Outline each blood parasite and name the species.
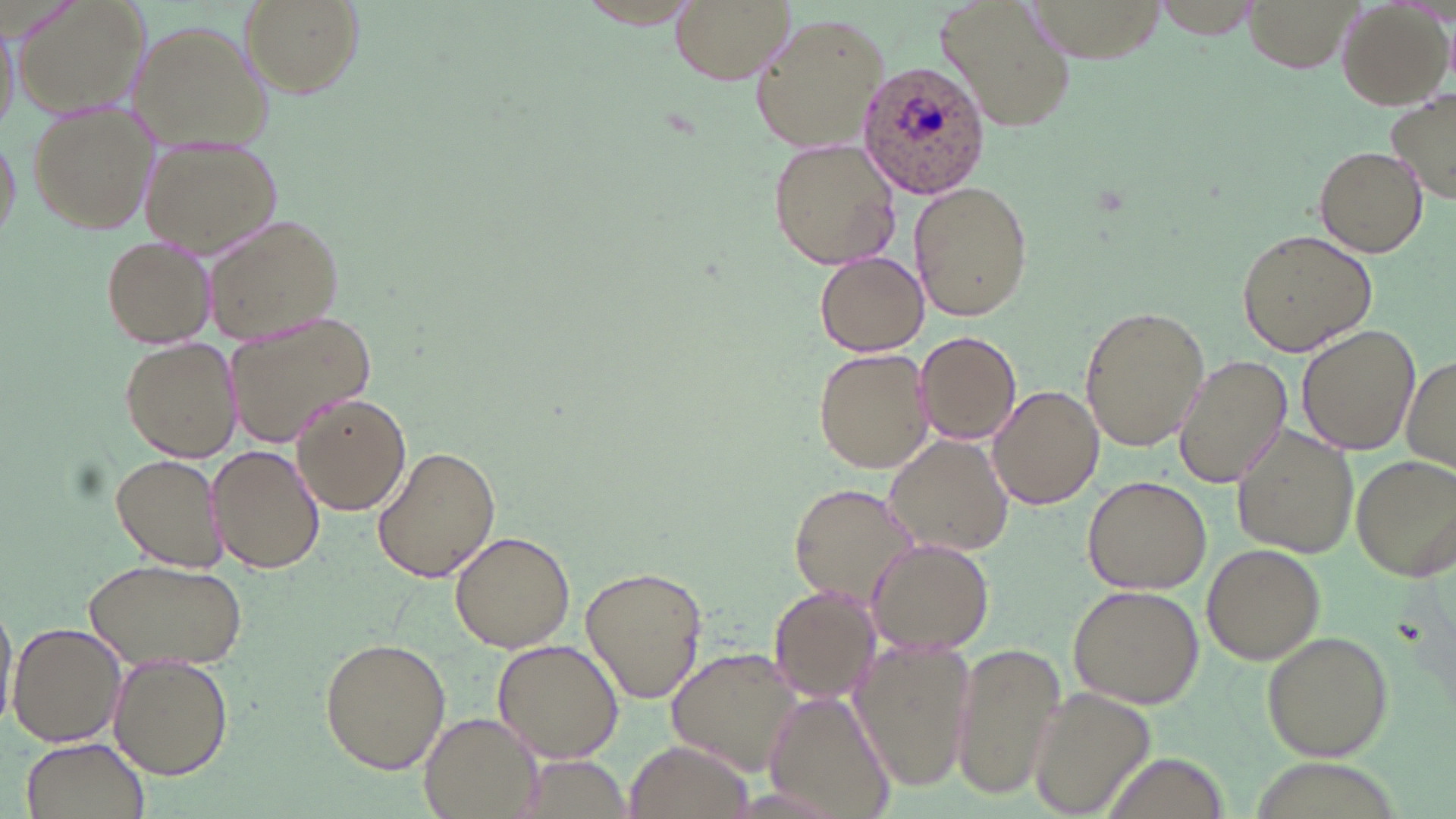

Approximate bounding boxes as named x1/y1/x2/y2 corners in pixels.
Plasmodium ovale-infected red blood cells: (x1=858, y1=58, x2=990, y2=199).
No Plasmodium falciparum, Plasmodium malariae, Plasmodium vivax, Babesia divergens, or Trypanosoma brucei observed.

Uninfected red blood cell locations: (x1=14, y1=0, x2=151, y2=118), (x1=669, y1=0, x2=795, y2=84), (x1=934, y1=0, x2=1079, y2=132), (x1=1155, y1=0, x2=1265, y2=40), (x1=1247, y1=0, x2=1354, y2=72), (x1=238, y1=1, x2=362, y2=98), (x1=1336, y1=2, x2=1451, y2=110), (x1=1, y1=10, x2=20, y2=140), (x1=749, y1=14, x2=888, y2=155), (x1=128, y1=19, x2=272, y2=153), (x1=1387, y1=93, x2=1455, y2=204), (x1=25, y1=103, x2=157, y2=232), (x1=141, y1=135, x2=282, y2=258), (x1=768, y1=137, x2=901, y2=270), (x1=1313, y1=145, x2=1429, y2=256), (x1=909, y1=180, x2=1033, y2=323), (x1=201, y1=213, x2=346, y2=341), (x1=1236, y1=227, x2=1379, y2=358), (x1=100, y1=234, x2=216, y2=349), (x1=815, y1=252, x2=929, y2=355), (x1=1080, y1=305, x2=1209, y2=453), (x1=222, y1=311, x2=378, y2=447), (x1=1297, y1=324, x2=1420, y2=454), (x1=916, y1=330, x2=1021, y2=445), (x1=121, y1=337, x2=241, y2=462), (x1=813, y1=347, x2=934, y2=474), (x1=1172, y1=353, x2=1292, y2=488), (x1=1402, y1=353, x2=1456, y2=476), (x1=987, y1=384, x2=1103, y2=509), (x1=292, y1=393, x2=412, y2=516), (x1=1233, y1=426, x2=1357, y2=558), (x1=884, y1=436, x2=1016, y2=557), (x1=207, y1=444, x2=327, y2=574), (x1=371, y1=445, x2=501, y2=585), (x1=109, y1=452, x2=227, y2=573), (x1=1352, y1=454, x2=1456, y2=579), (x1=1080, y1=476, x2=1209, y2=593), (x1=788, y1=482, x2=921, y2=611), (x1=449, y1=532, x2=576, y2=652), (x1=867, y1=539, x2=993, y2=655), (x1=1202, y1=543, x2=1325, y2=663), (x1=85, y1=557, x2=249, y2=672), (x1=579, y1=566, x2=709, y2=703), (x1=768, y1=584, x2=881, y2=701), (x1=1068, y1=584, x2=1205, y2=709), (x1=0, y1=596, x2=17, y2=736), (x1=7, y1=622, x2=126, y2=749), (x1=1260, y1=631, x2=1393, y2=762), (x1=851, y1=634, x2=978, y2=794), (x1=319, y1=637, x2=451, y2=774), (x1=493, y1=639, x2=624, y2=762), (x1=951, y1=641, x2=1065, y2=801), (x1=666, y1=648, x2=811, y2=778), (x1=109, y1=653, x2=232, y2=778), (x1=1025, y1=686, x2=1156, y2=819), (x1=761, y1=692, x2=893, y2=818), (x1=422, y1=714, x2=540, y2=819), (x1=20, y1=736, x2=146, y2=817), (x1=621, y1=739, x2=755, y2=819), (x1=519, y1=754, x2=626, y2=818). Slide-level diagnosis: Plasmodium ovale. Light microscopy. One field of a larger specimen. Image is 1456×819 pixels. 1000x magnification. Thin blood smear. May-Grünwald-Giemsa stain.